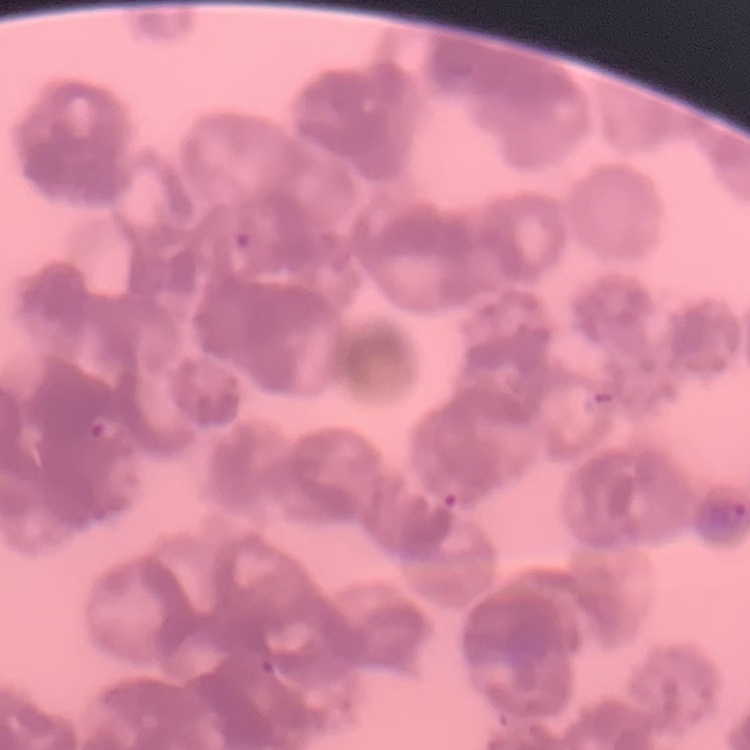
erythrocyte_morphology: rouleaux formation
stain: Field's or Giemsa
preparation: thin blood film
image_type: one tile cut from a larger photomicrograph